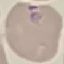 Malaria status: parasitized. Acquired by smartphone through the microscope eyepiece. Automatically extracted cell patch, resized to 64 × 64 pixels. Thin blood film. Giemsa-stained preparation.